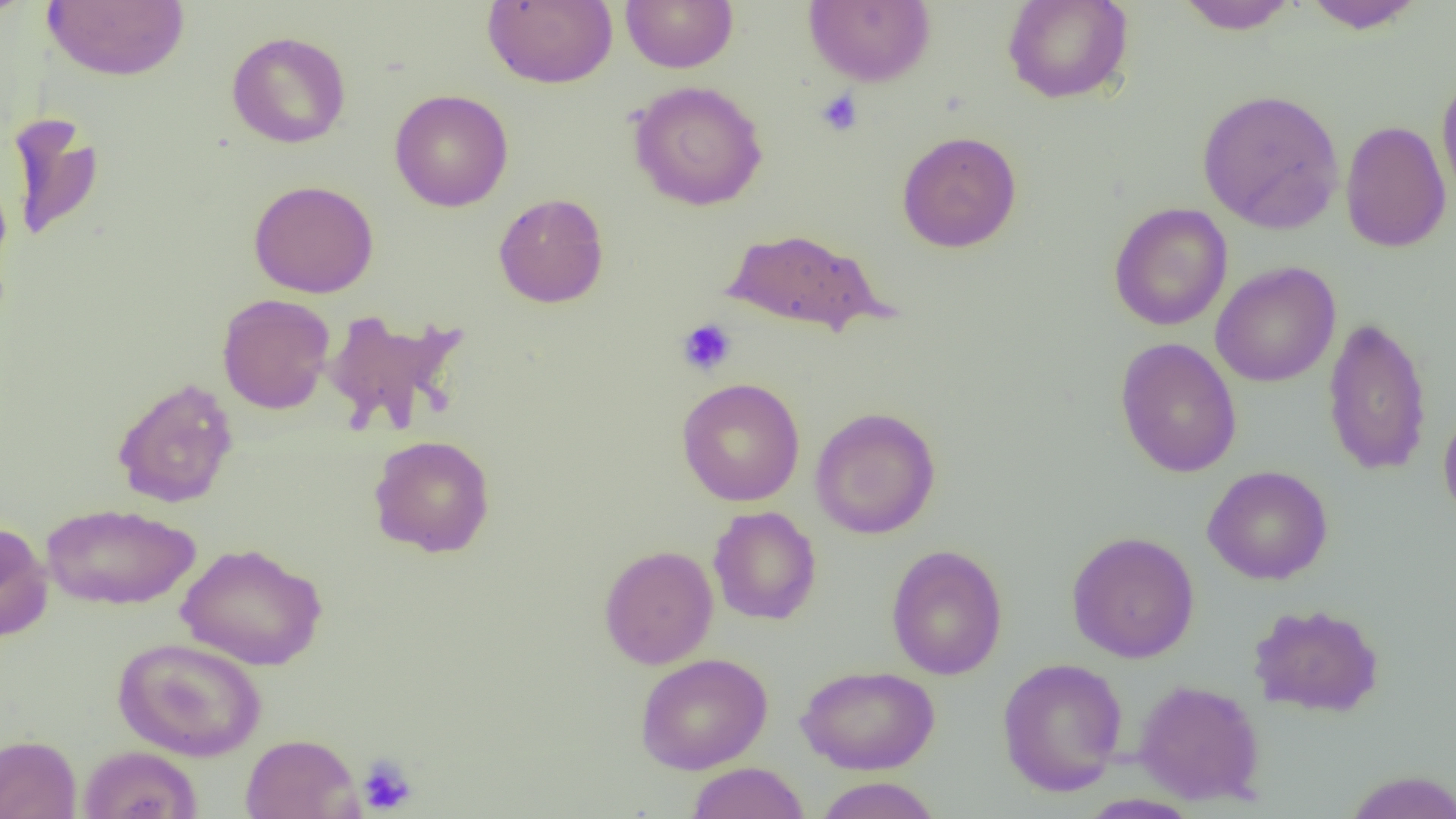 Approximate bounding boxes as named x1/y1/x2/y2 corners in pixels. Platelet locations: (x1=815, y1=89, x2=863, y2=136), (x1=677, y1=318, x2=737, y2=377), (x1=356, y1=755, x2=418, y2=816). Uninfected red blood cell locations: (x1=0, y1=0, x2=35, y2=23), (x1=482, y1=0, x2=617, y2=88), (x1=620, y1=0, x2=738, y2=73), (x1=803, y1=0, x2=936, y2=87), (x1=1002, y1=0, x2=1134, y2=104), (x1=1301, y1=0, x2=1426, y2=33), (x1=42, y1=1, x2=190, y2=81), (x1=1174, y1=1, x2=1301, y2=34), (x1=226, y1=31, x2=351, y2=149), (x1=1436, y1=71, x2=1456, y2=210), (x1=628, y1=80, x2=768, y2=211), (x1=1197, y1=88, x2=1344, y2=233), (x1=389, y1=89, x2=514, y2=212), (x1=5, y1=112, x2=105, y2=243), (x1=1340, y1=119, x2=1452, y2=254), (x1=896, y1=131, x2=1022, y2=253), (x1=248, y1=179, x2=379, y2=298), (x1=493, y1=193, x2=609, y2=308), (x1=1108, y1=202, x2=1233, y2=331), (x1=721, y1=227, x2=887, y2=336), (x1=1211, y1=261, x2=1341, y2=387), (x1=217, y1=294, x2=334, y2=414), (x1=321, y1=308, x2=469, y2=438), (x1=1321, y1=315, x2=1432, y2=477), (x1=1114, y1=337, x2=1242, y2=478), (x1=111, y1=377, x2=239, y2=509), (x1=677, y1=377, x2=805, y2=506), (x1=1438, y1=401, x2=1456, y2=525), (x1=810, y1=406, x2=941, y2=540), (x1=368, y1=434, x2=496, y2=558), (x1=1203, y1=465, x2=1333, y2=585), (x1=41, y1=503, x2=200, y2=611), (x1=708, y1=506, x2=822, y2=625), (x1=0, y1=520, x2=53, y2=643), (x1=1066, y1=531, x2=1200, y2=663), (x1=175, y1=543, x2=327, y2=670), (x1=885, y1=544, x2=1008, y2=680), (x1=598, y1=545, x2=719, y2=669), (x1=1248, y1=602, x2=1385, y2=718), (x1=113, y1=636, x2=266, y2=761), (x1=635, y1=653, x2=773, y2=775), (x1=996, y1=657, x2=1128, y2=797), (x1=796, y1=664, x2=940, y2=775), (x1=1133, y1=679, x2=1266, y2=806), (x1=240, y1=733, x2=362, y2=818), (x1=0, y1=734, x2=82, y2=819), (x1=78, y1=745, x2=203, y2=819), (x1=686, y1=762, x2=810, y2=819), (x1=1342, y1=769, x2=1456, y2=819), (x1=814, y1=776, x2=941, y2=819), (x1=1078, y1=793, x2=1203, y2=818). Slide-level diagnosis: negative for blood parasites. Image is 1456×819 pixels. Captured at 1000x magnification. Single field of view. Light microscopy. Thin blood film.